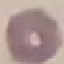
Malaria status: uninfected. Acquired by smartphone through the microscope eyepiece. Giemsa stain. Cell patch, automatically extracted from a larger field of view and resized to 64 × 64 pixels. Thin blood smear.